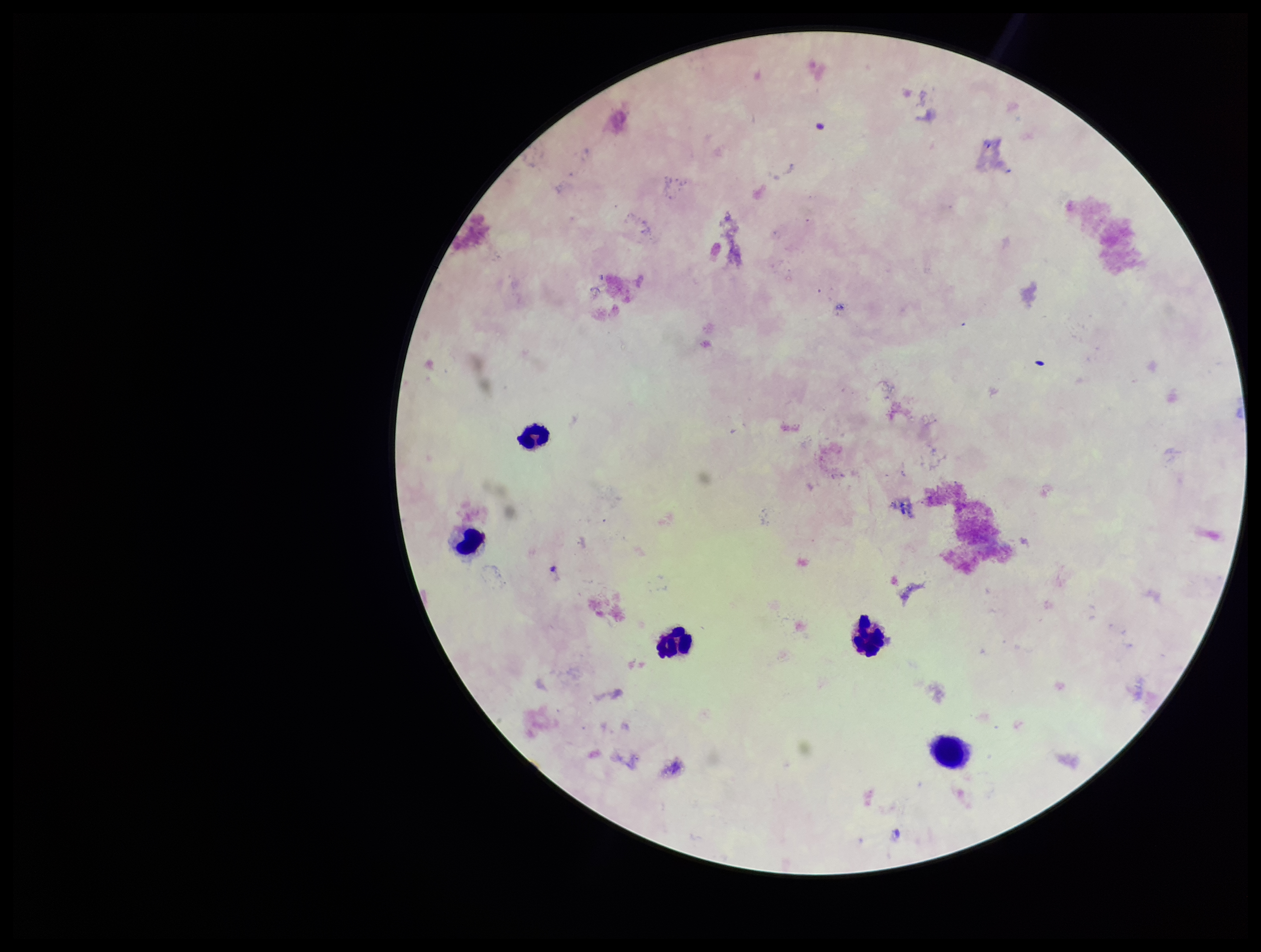
Photographed through the microscope eyepiece with a smartphone camera. One field from this slide. Leukocyte count: 5. Preparation: thick. Stained with Giemsa. Plasmodium parasites: none identified. Image is 1261×952 pixels. Patient malaria status: positive. Parasite count: 0. Species reported for this patient: Plasmodium falciparum.